Classify this cell by malaria status.
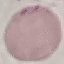

It is uninfected.

stain = Giemsa
capture = smartphone through the microscope eyepiece
preparation = thin blood film
image type = automatically extracted cell patch, resized to 64 × 64 pixels